Outline each Plasmodium ovale-infected red blood cell.
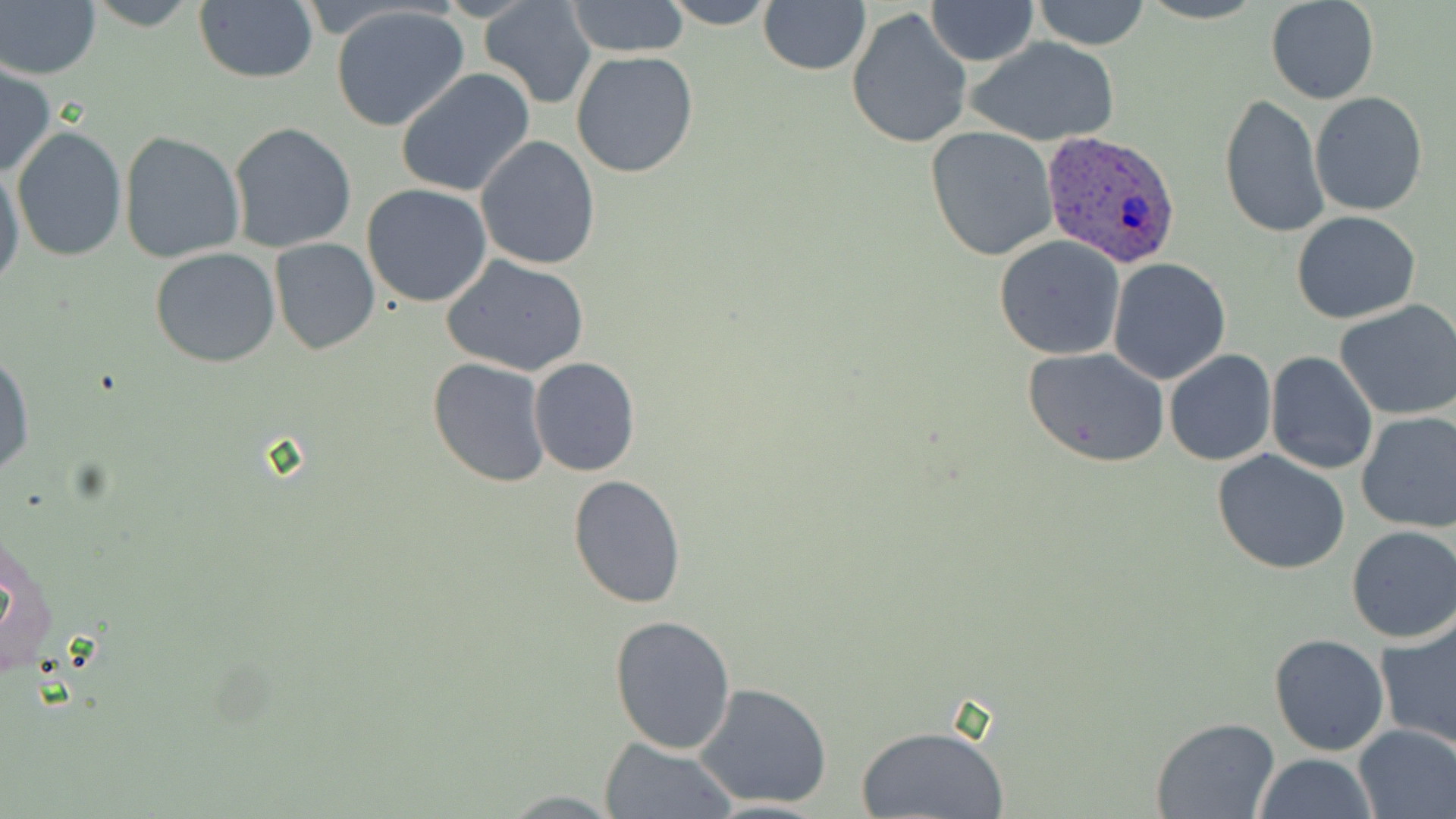

Approximate bounding boxes as named x1/y1/x2/y2 corners in pixels.
Plasmodium ovale-infected red blood cells: (x1=1043, y1=131, x2=1179, y2=269).

slide-level diagnosis = Plasmodium ovale
field of view = single
uninfected red blood cell locations = approximate bounding boxes as named x1/y1/x2/y2 corners in pixels: (x1=0, y1=0, x2=101, y2=82), (x1=82, y1=0, x2=206, y2=31), (x1=479, y1=0, x2=596, y2=110), (x1=656, y1=0, x2=781, y2=28), (x1=925, y1=0, x2=1038, y2=65), (x1=1033, y1=0, x2=1149, y2=49), (x1=1265, y1=0, x2=1379, y2=104), (x1=192, y1=1, x2=319, y2=87), (x1=565, y1=1, x2=691, y2=58), (x1=758, y1=2, x2=871, y2=76), (x1=329, y1=4, x2=473, y2=134), (x1=846, y1=6, x2=974, y2=150), (x1=965, y1=38, x2=1119, y2=146), (x1=570, y1=51, x2=699, y2=178), (x1=0, y1=61, x2=55, y2=179), (x1=394, y1=67, x2=536, y2=196), (x1=1218, y1=92, x2=1329, y2=240), (x1=1310, y1=92, x2=1428, y2=216), (x1=226, y1=121, x2=359, y2=253), (x1=10, y1=126, x2=127, y2=263), (x1=924, y1=126, x2=1058, y2=262), (x1=118, y1=131, x2=245, y2=265), (x1=475, y1=136, x2=601, y2=271), (x1=1, y1=162, x2=24, y2=288), (x1=361, y1=184, x2=493, y2=307), (x1=1292, y1=211, x2=1421, y2=324), (x1=994, y1=234, x2=1126, y2=359), (x1=269, y1=237, x2=379, y2=355), (x1=150, y1=247, x2=281, y2=368), (x1=441, y1=253, x2=590, y2=377), (x1=1108, y1=257, x2=1231, y2=385), (x1=1336, y1=300, x2=1456, y2=420), (x1=1285, y1=315, x2=1435, y2=449), (x1=1022, y1=346, x2=1171, y2=468), (x1=0, y1=349, x2=34, y2=481), (x1=1163, y1=350, x2=1276, y2=466), (x1=1264, y1=351, x2=1379, y2=476), (x1=427, y1=357, x2=552, y2=488), (x1=530, y1=357, x2=641, y2=477), (x1=1355, y1=409, x2=1456, y2=532), (x1=1211, y1=448, x2=1351, y2=576), (x1=566, y1=476, x2=687, y2=609), (x1=4, y1=521, x2=60, y2=687), (x1=1346, y1=527, x2=1456, y2=643), (x1=609, y1=614, x2=738, y2=754), (x1=1376, y1=617, x2=1456, y2=751), (x1=1268, y1=633, x2=1391, y2=756), (x1=694, y1=682, x2=836, y2=810), (x1=1151, y1=717, x2=1278, y2=819), (x1=855, y1=724, x2=1010, y2=818), (x1=1353, y1=725, x2=1456, y2=818), (x1=600, y1=739, x2=736, y2=819), (x1=1252, y1=754, x2=1379, y2=818)
magnification = 1000x
modality = optical microscopy
stain = May-Grünwald-Giemsa
preparation = thin blood smear
image size = 1456×819 pixels